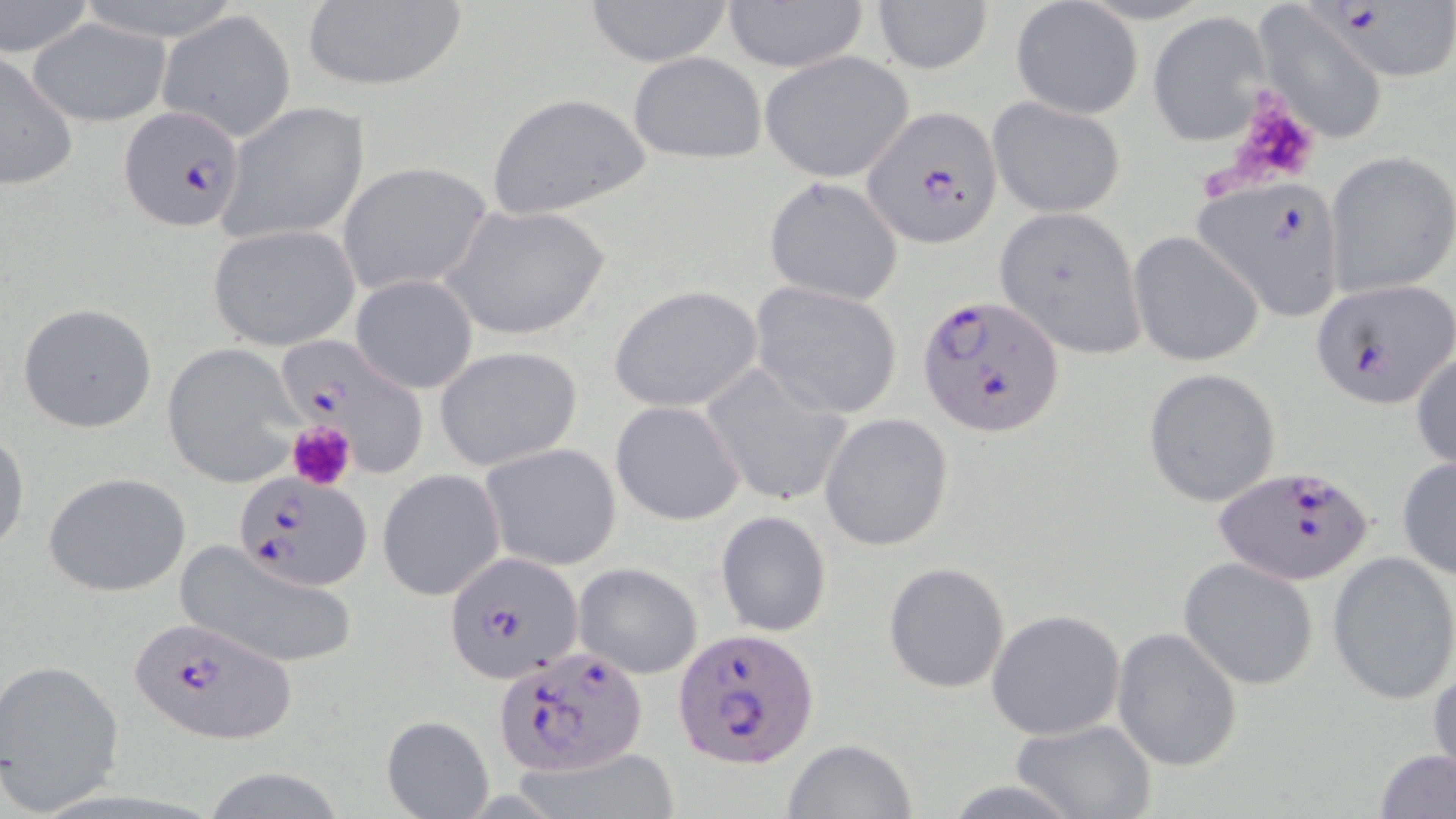
Approximate bounding boxes as [x1, y1, x2, y2] in pixels. Platelet locations: [1222, 89, 1319, 191], [287, 420, 356, 492]. Plasmodium falciparum-infected red blood cell locations: [1306, 2, 1455, 83], [117, 106, 248, 233], [862, 109, 1003, 249], [1195, 180, 1346, 320], [1311, 278, 1453, 407], [917, 292, 1065, 435], [275, 336, 428, 473], [1215, 466, 1376, 584], [235, 468, 372, 591], [443, 550, 583, 684], [126, 616, 296, 745], [671, 627, 820, 766], [492, 646, 648, 777]. Uninfected red blood cell locations: [582, 0, 735, 67], [717, 0, 873, 71], [0, 1, 94, 61], [299, 1, 468, 92], [870, 1, 991, 74], [1012, 1, 1142, 120], [1252, 2, 1389, 145], [158, 10, 297, 142], [1147, 12, 1271, 146], [26, 16, 171, 125], [629, 51, 766, 164], [759, 51, 915, 181], [0, 52, 76, 194], [485, 92, 651, 220], [987, 96, 1126, 218], [218, 101, 371, 246], [1323, 151, 1456, 299], [337, 161, 492, 299], [763, 177, 904, 306], [443, 201, 612, 342], [994, 207, 1146, 360], [207, 223, 359, 350], [1127, 230, 1265, 369], [351, 275, 478, 394], [749, 282, 904, 419], [608, 284, 763, 414], [16, 303, 158, 433], [161, 343, 303, 487], [1410, 343, 1456, 476], [433, 344, 582, 471], [700, 362, 853, 507], [1141, 366, 1282, 508], [610, 400, 746, 526], [819, 413, 954, 552], [1, 430, 29, 557], [480, 442, 622, 570], [1396, 455, 1456, 582], [377, 470, 506, 601], [43, 472, 192, 597], [715, 510, 832, 636], [174, 538, 361, 670], [1326, 550, 1456, 704], [1177, 556, 1320, 690], [881, 561, 1011, 692], [573, 563, 703, 679], [986, 609, 1127, 741], [1111, 626, 1243, 773], [1428, 654, 1456, 785], [0, 658, 126, 812], [382, 715, 493, 819], [1009, 718, 1158, 819], [781, 739, 918, 819], [1373, 747, 1456, 819], [195, 765, 354, 819], [940, 779, 1084, 817]. Slide-level diagnosis: Plasmodium falciparum. Light microscopy. Image is 1456×819 pixels. Single field of view. Captured at 1000x magnification. May-Grünwald-Giemsa stain. Thin blood smear.